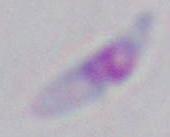

identification: Toxoplasma gondii
modality: micrograph
magnification: 1000x